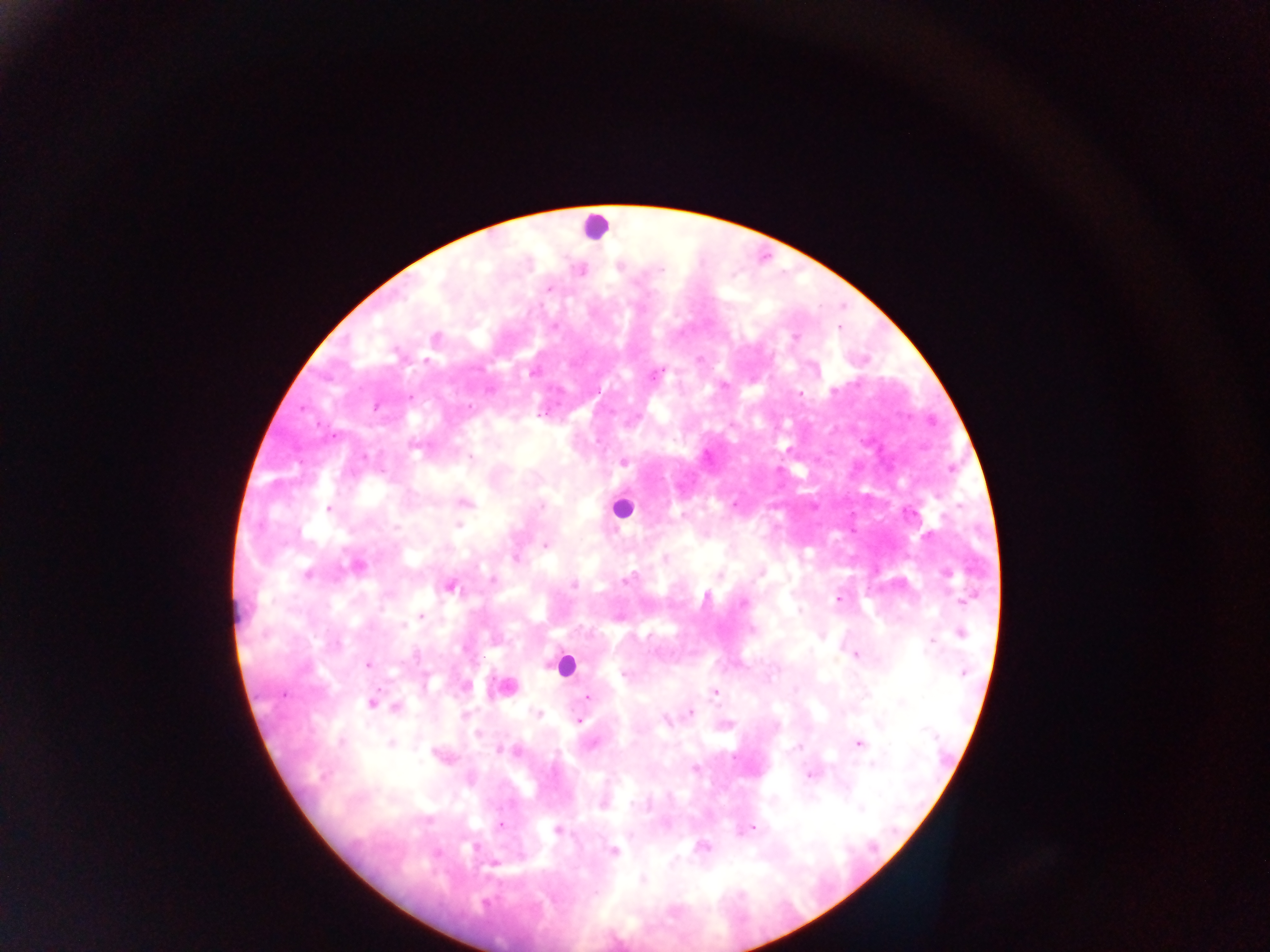
Approximate centers as x y in pixels.
Summary:
  - Leukocyte locations: 594 227; 621 508; 564 665
  - Malaria parasite locations: 661 269; 550 289; 555 326; 839 327; 794 337; 699 360; 426 361; 532 373; 653 376; 833 390; 800 394; 409 397; 376 406; 470 407; 302 408; 334 436; 415 446; 364 456; 472 458; 624 462; 466 503; 733 505; 541 506; 328 509; 683 515; 458 525; 546 545; 515 558; 665 558; 357 566; 307 574; 760 574; 946 574; 718 576; 493 580; 627 580; 574 585; 450 587; 706 598; 837 599; 962 602; 742 604; 799 611; 421 616; 403 625; 961 634; 931 642; 338 643; 856 654; 368 665; 625 674; 962 674; 505 688; 715 692; 588 696; 371 703; 902 703; 396 707; 538 713; 690 713; 465 714; 578 721; 666 722; 478 733; 341 742; 391 744; 591 744; 859 744; 799 746; 499 750; 518 751; 873 763; 695 769; 808 775; 603 806; 861 808; 500 825; 752 828; 557 830; 702 847; 475 848; 614 850; 494 864; 642 880
  - Preparation: thick blood film
  - Field of view: single
  - Country: Ghana
  - Capture: mobile-phone photograph through a microscope
  - Image size: 1270×952 pixels